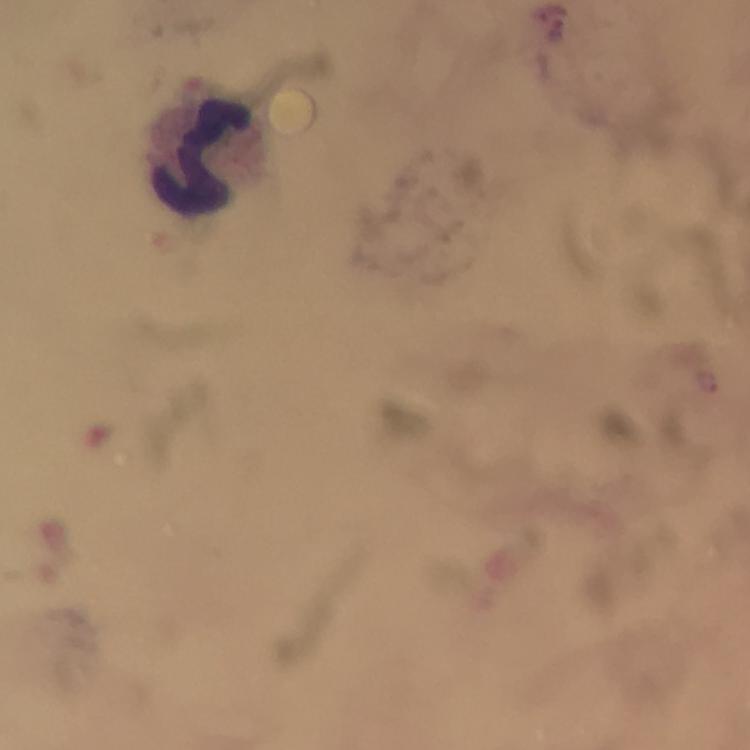

image size = 750×750 pixels
cropped from = one field of view
immersion oil = used
magnification = 100x
context = from a diagnostic examination for malaria
preparation = thick smear
leukocyte locations = approximate object centers, in pixels from the top-left corner: (x=201, y=159)
stain = Giemsa
malaria parasite locations = approximate object centers, in pixels from the top-left corner: (x=558, y=28)
capture = smartphone photograph through a microscope